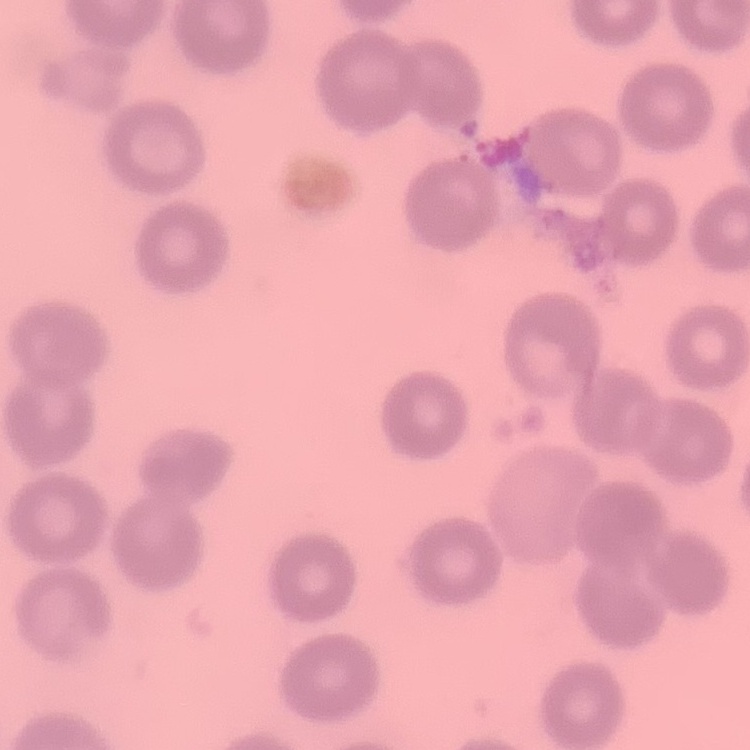
red blood cell morphology = no rouleaux formation
stain = Field's or Giemsa
image type = one tile cut from a larger photomicrograph
preparation = thin peripheral smear